Identify the parasite.
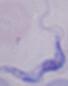

This is a trypanosome.

modality = photomicrograph
magnification = 1000x